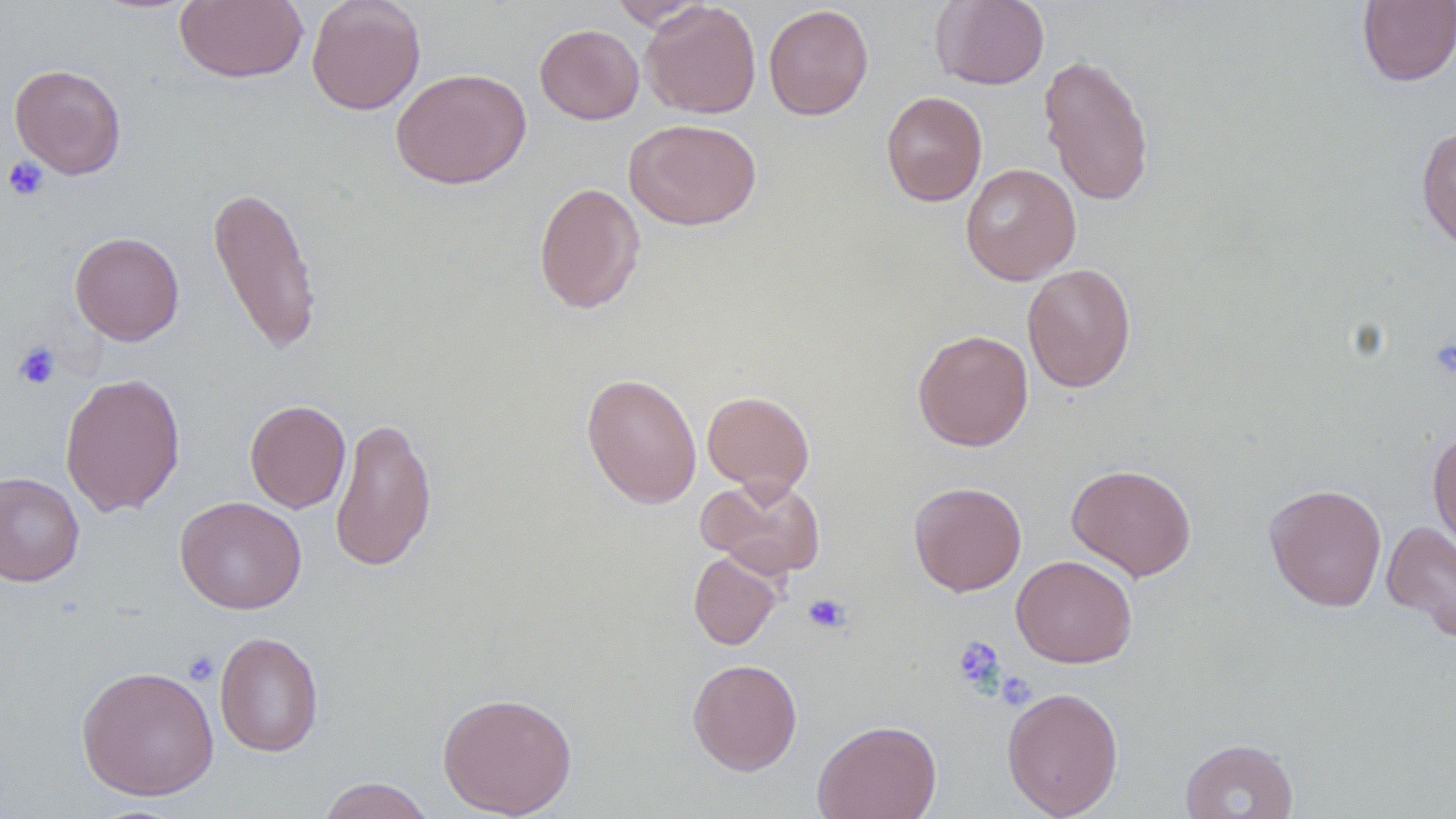

Approximate bounding boxes as (x1,y1)-(x2,y2) corner pairs in pixels. Platelet locations: (2,156)-(50,201), (1429,338)-(1456,380), (12,342)-(61,389), (803,593)-(850,633), (952,636)-(1005,693), (183,650)-(220,686), (996,670)-(1037,710). Uninfected red blood cell locations: (174,0)-(308,84), (306,0)-(426,114), (930,0)-(1049,90), (1357,0)-(1456,87), (608,1)-(712,31), (641,1)-(761,119), (763,4)-(874,120), (535,24)-(644,124), (1038,53)-(1155,207), (9,63)-(127,179), (390,68)-(531,189), (881,91)-(987,207), (624,118)-(762,230), (1416,125)-(1456,255), (960,163)-(1081,285), (533,181)-(646,315), (206,183)-(323,356), (69,231)-(185,345), (1022,263)-(1136,393), (912,328)-(1034,452), (59,372)-(186,516), (582,372)-(702,509), (702,390)-(815,496), (244,399)-(351,513), (330,415)-(437,572), (1428,430)-(1456,552), (1066,463)-(1197,580), (0,471)-(84,586), (698,475)-(827,579), (909,481)-(1027,596), (1263,482)-(1387,612), (175,496)-(306,614), (1381,520)-(1456,643), (689,551)-(782,650), (1011,554)-(1137,668), (214,631)-(323,757), (687,658)-(803,775), (76,664)-(219,801), (1002,686)-(1124,818), (437,691)-(577,818), (812,719)-(942,819), (1180,738)-(1299,819), (316,777)-(435,819). Slide-level diagnosis: no evidence of blood parasites. Single field of view. May-Grünwald-Giemsa stain. Optical microscopy. Image is 1456×819 pixels. Thin blood smear. 1000x magnification.